Locate every uninfected red blood cell.
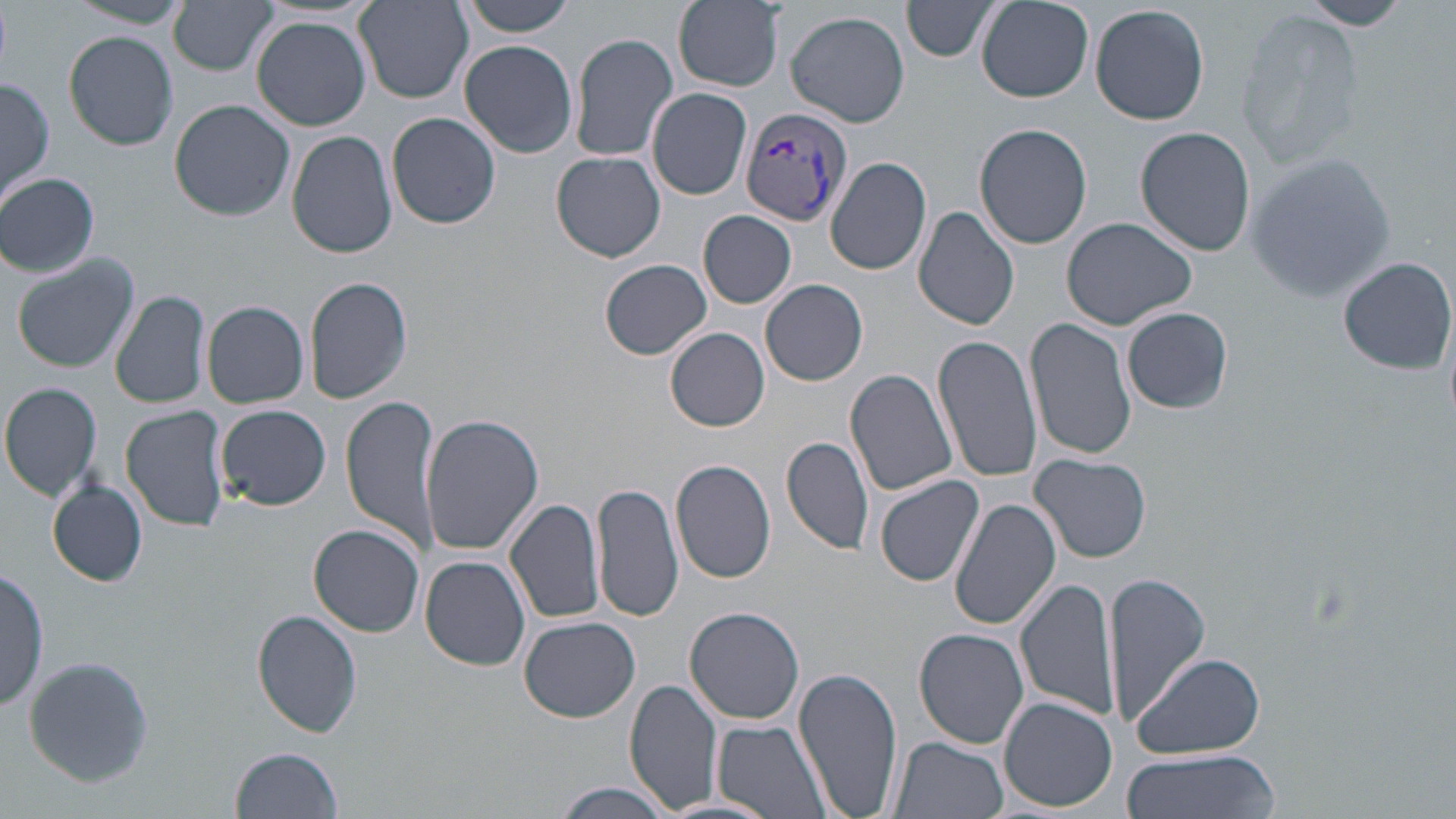
Approximate bounding boxes as [x1, y1, x2, y2] in pixels.
Uninfected red blood cells: [67, 0, 191, 28], [458, 0, 581, 36], [670, 0, 790, 94], [902, 0, 1003, 61], [976, 0, 1094, 102], [1304, 0, 1416, 30], [169, 1, 279, 76], [354, 1, 473, 103], [1091, 3, 1210, 126], [1235, 7, 1365, 168], [786, 9, 912, 128], [251, 15, 372, 131], [63, 29, 179, 151], [568, 30, 679, 162], [459, 40, 580, 159], [1, 76, 55, 208], [648, 87, 752, 200], [170, 100, 294, 221], [388, 111, 501, 230], [974, 124, 1092, 249], [1135, 126, 1255, 256], [288, 131, 397, 259], [552, 152, 666, 262], [1243, 153, 1400, 303], [826, 156, 933, 277], [0, 173, 99, 278], [913, 205, 1020, 331], [699, 211, 797, 308], [1060, 217, 1199, 331], [10, 253, 141, 373], [1337, 256, 1455, 373], [600, 259, 713, 359], [304, 275, 414, 405], [760, 279, 868, 386], [111, 289, 209, 410], [202, 300, 310, 408], [1122, 307, 1234, 414], [1027, 316, 1137, 461], [666, 328, 770, 432], [932, 334, 1044, 483], [845, 368, 959, 498], [0, 381, 103, 501], [343, 394, 441, 554], [216, 403, 331, 511], [120, 404, 230, 533], [418, 412, 543, 555], [782, 435, 875, 556], [1030, 453, 1151, 564], [671, 458, 777, 584], [875, 474, 987, 587], [48, 479, 148, 588], [591, 481, 683, 622], [951, 495, 1062, 630], [506, 499, 606, 625], [441, 515, 586, 641], [308, 524, 424, 637], [421, 556, 531, 671], [1110, 570, 1209, 728], [0, 571, 47, 710], [1015, 576, 1118, 724], [686, 607, 805, 725], [252, 608, 362, 737], [519, 616, 641, 723], [914, 629, 1029, 749], [1131, 650, 1267, 760], [25, 656, 155, 789], [794, 666, 903, 819], [626, 679, 722, 814], [999, 697, 1115, 812], [711, 718, 835, 819], [888, 736, 1008, 819], [231, 747, 345, 819], [1120, 750, 1280, 819], [551, 782, 673, 819], [659, 797, 781, 819].

Plasmodium vivax-infected red blood cell locations: [740, 107, 854, 227]. Slide-level diagnosis: Plasmodium vivax. Light microscopy. 1000x magnification. Thin blood film. Single field of view. Image is 1456×819 pixels. May-Grünwald-Giemsa-stained preparation.